Report the malaria status of this cell.
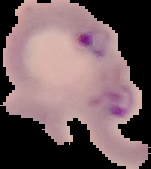

Parasitized.

Image is 151×169 pixels. Cell region segmented out of the field of view; the surrounding area is masked to black. From a thin blood smear.